Assess the morphology of the erythrocytes.
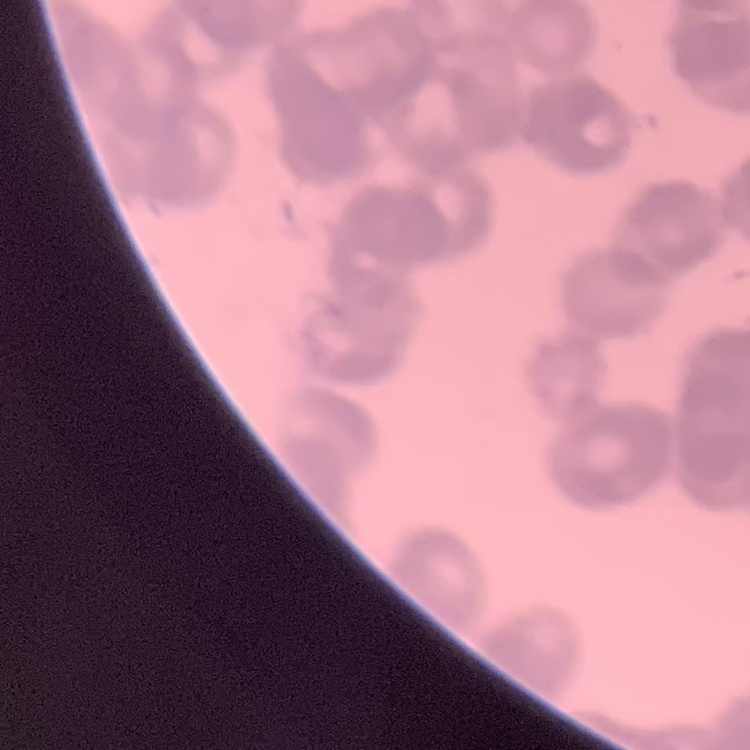

Rouleaux formation.

Thin peripheral smear. One tile cut from a larger photomicrograph. Field's or Giemsa stain.